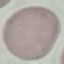

Summary:
  - Malaria status: uninfected
  - Stain: Giemsa
  - Preparation: thin smear
  - Image type: cell patch, automatically extracted from a larger field of view and resized to 64 × 64 pixels
  - Capture: smartphone through the microscope eyepiece